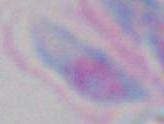

magnification = 1000x
identification = Toxoplasma gondii
modality = micrograph